Assess this cell for malaria.
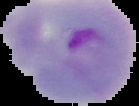
It is parasitized.

Segmented cell region on a black background. Image is 139×106 pixels. From a thin blood film.